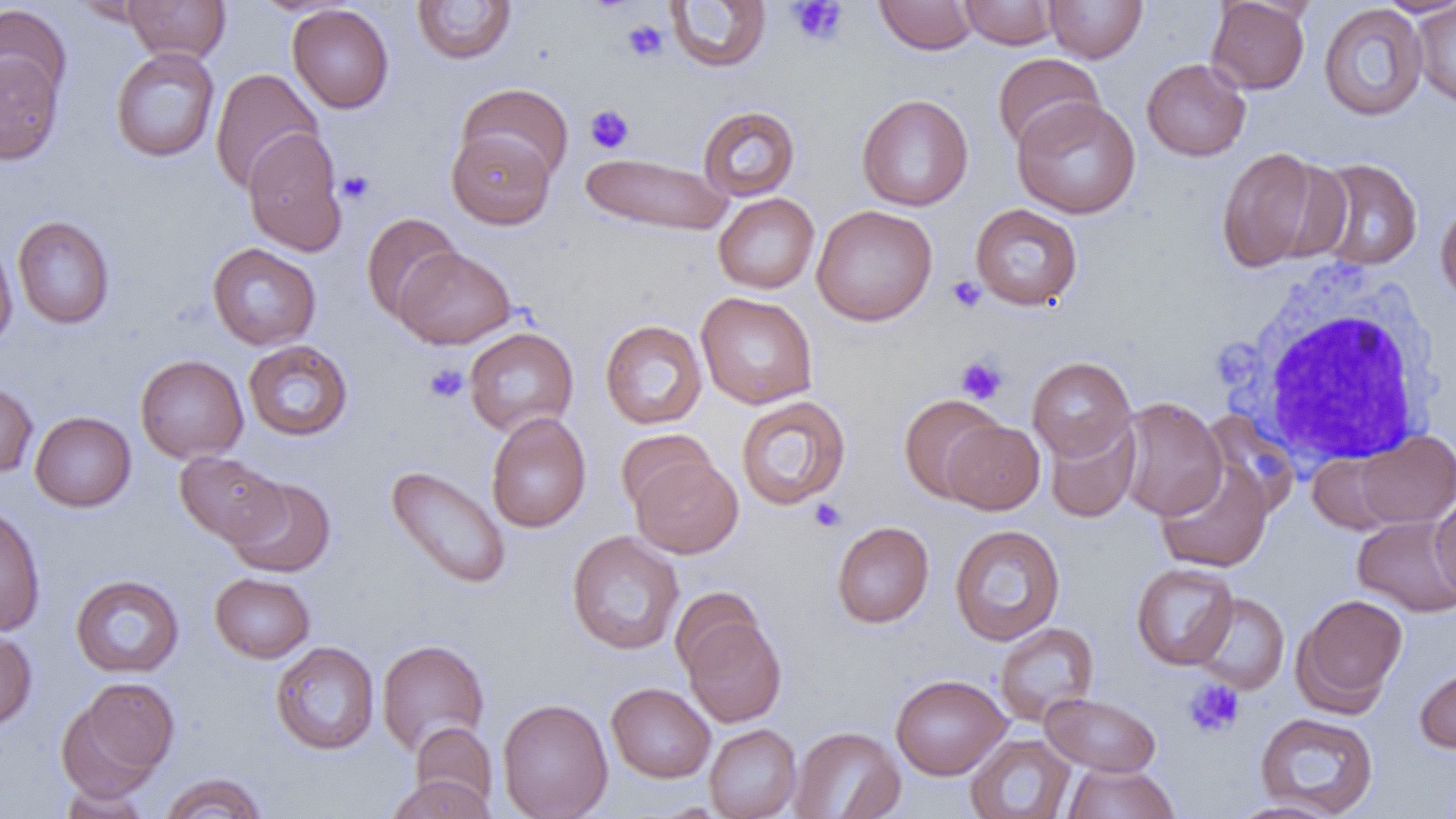
Summary:
  - Coordinate format: approximate bounding boxes as [x1, y1, x2, y2] in pixels
  - Platelet locations: [787, 1, 848, 46], [622, 19, 669, 61], [585, 105, 634, 154], [337, 170, 374, 205], [946, 275, 987, 313], [955, 356, 1008, 405], [424, 363, 469, 403], [810, 499, 846, 532], [1183, 678, 1244, 738]
  - White blood cell locations: [1224, 259, 1445, 470]
  - Uninfected red blood cell locations: [72, 0, 161, 26], [122, 0, 230, 63], [875, 0, 979, 54], [959, 0, 1060, 49], [1044, 0, 1147, 63], [1376, 0, 1456, 17], [412, 1, 517, 65], [664, 1, 772, 73], [1206, 1, 1311, 94], [1411, 1, 1456, 109], [0, 4, 72, 108], [287, 4, 394, 114], [1318, 4, 1428, 121], [110, 47, 220, 163], [0, 52, 64, 164], [992, 53, 1105, 152], [1142, 58, 1251, 161], [210, 68, 323, 194], [457, 83, 574, 184], [857, 94, 973, 212], [1011, 96, 1142, 219], [697, 105, 801, 201], [242, 127, 348, 256], [447, 129, 556, 229], [1215, 147, 1339, 272], [581, 151, 733, 237], [1309, 157, 1423, 271], [713, 193, 820, 294], [1435, 199, 1456, 307], [970, 203, 1083, 310], [811, 204, 938, 326], [361, 212, 462, 322], [12, 215, 115, 329], [0, 237, 18, 352], [207, 243, 321, 350], [395, 246, 516, 349], [695, 292, 819, 409], [600, 319, 707, 429], [464, 327, 579, 436], [243, 339, 353, 441], [135, 354, 248, 463], [1027, 356, 1136, 461], [0, 379, 38, 479], [735, 395, 852, 510], [899, 395, 1006, 503], [1115, 397, 1227, 521], [1199, 410, 1299, 518], [29, 411, 136, 511], [486, 412, 591, 533], [1043, 417, 1140, 523], [942, 420, 1045, 514], [615, 429, 717, 514], [1354, 430, 1456, 528], [175, 451, 287, 547], [1308, 453, 1401, 534], [630, 454, 744, 558], [1155, 458, 1274, 572], [386, 465, 511, 589], [226, 476, 337, 577], [1430, 492, 1456, 599], [0, 502, 45, 636], [1352, 516, 1456, 617], [831, 521, 934, 627], [949, 524, 1066, 645], [567, 530, 685, 655], [1131, 563, 1239, 669], [210, 572, 315, 663], [70, 574, 184, 678], [669, 586, 766, 679], [1190, 592, 1289, 694], [1293, 593, 1408, 712], [680, 615, 787, 727], [994, 622, 1099, 725], [0, 628, 37, 732], [376, 638, 490, 755], [270, 641, 380, 754], [1414, 662, 1456, 753], [890, 674, 1011, 779], [65, 678, 179, 792], [606, 682, 715, 782], [1040, 692, 1161, 777], [497, 698, 613, 819], [1254, 711, 1379, 817], [410, 721, 497, 810], [704, 724, 802, 819], [789, 726, 905, 819], [965, 734, 1075, 818], [1061, 762, 1179, 819], [159, 773, 268, 818], [387, 773, 494, 819], [59, 783, 151, 819], [1226, 800, 1344, 819]
  - Slide-level diagnosis: negative for blood parasites
  - Modality: optical microscopy
  - Preparation: thin blood film
  - Magnification: 1000x
  - Field of view: single
  - Image size: 1456×819 pixels